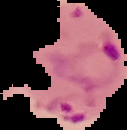

Summary:
  - Image type: cell region segmented out of the field of view; surrounding area masked to black
  - Result: malaria parasites detected
  - Preparation: thin blood film
  - Image size: 127×130 pixels